Comment on the morphology of the erythrocytes.
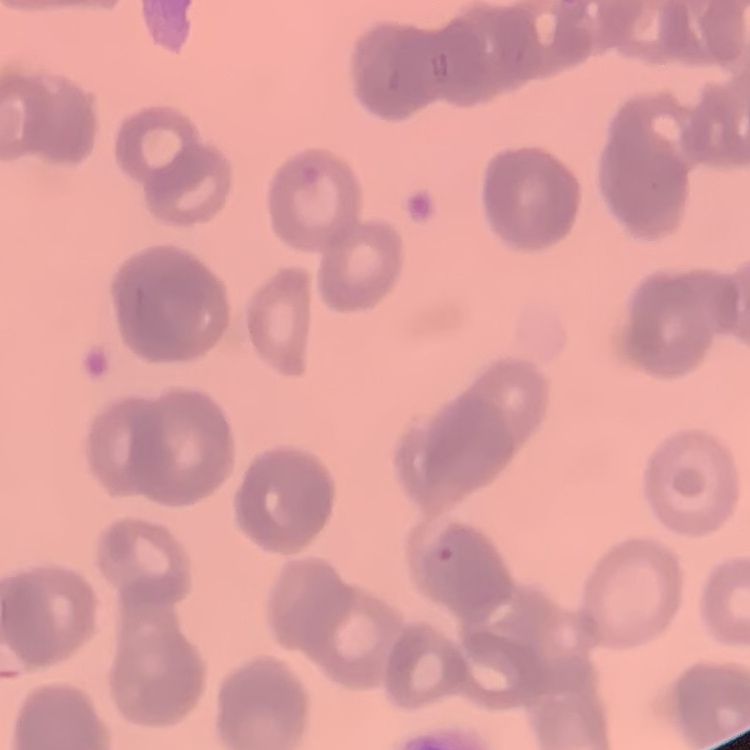
They show rouleaux formation.

stain = Field's or Giemsa
preparation = thin blood film
image type = square crop of a larger photomicrograph